State which cell type is depicted.
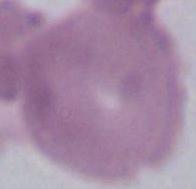

This is an erythrocyte.

modality = photomicrograph
magnification = 1000x